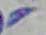
Toxoplasma gondii is seen. Micrograph. Captured at 1000x magnification.